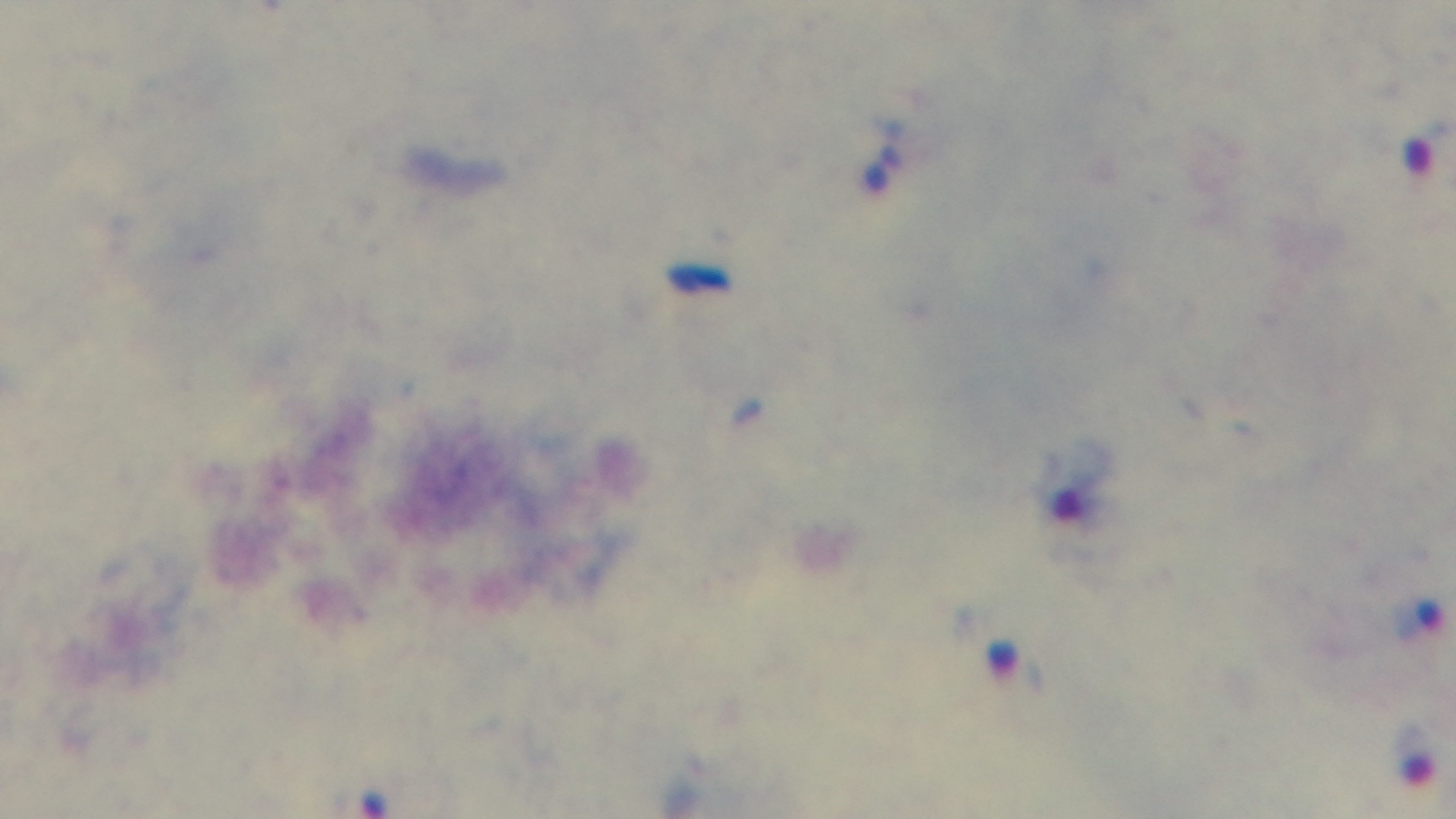 Photomicrograph. Preparation: thick. 100x oil-immersion objective. Single field of view. Malaria status: infected. Captured with a mounted 4K digital camera. Giemsa-stained.